Report the malaria status of this cell.
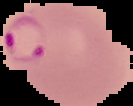
Parasitized.

Summary:
  - Image size: 133×106 pixels
  - Preparation: thin blood film
  - Image type: cell region segmented out of the field of view; surrounding area masked to black